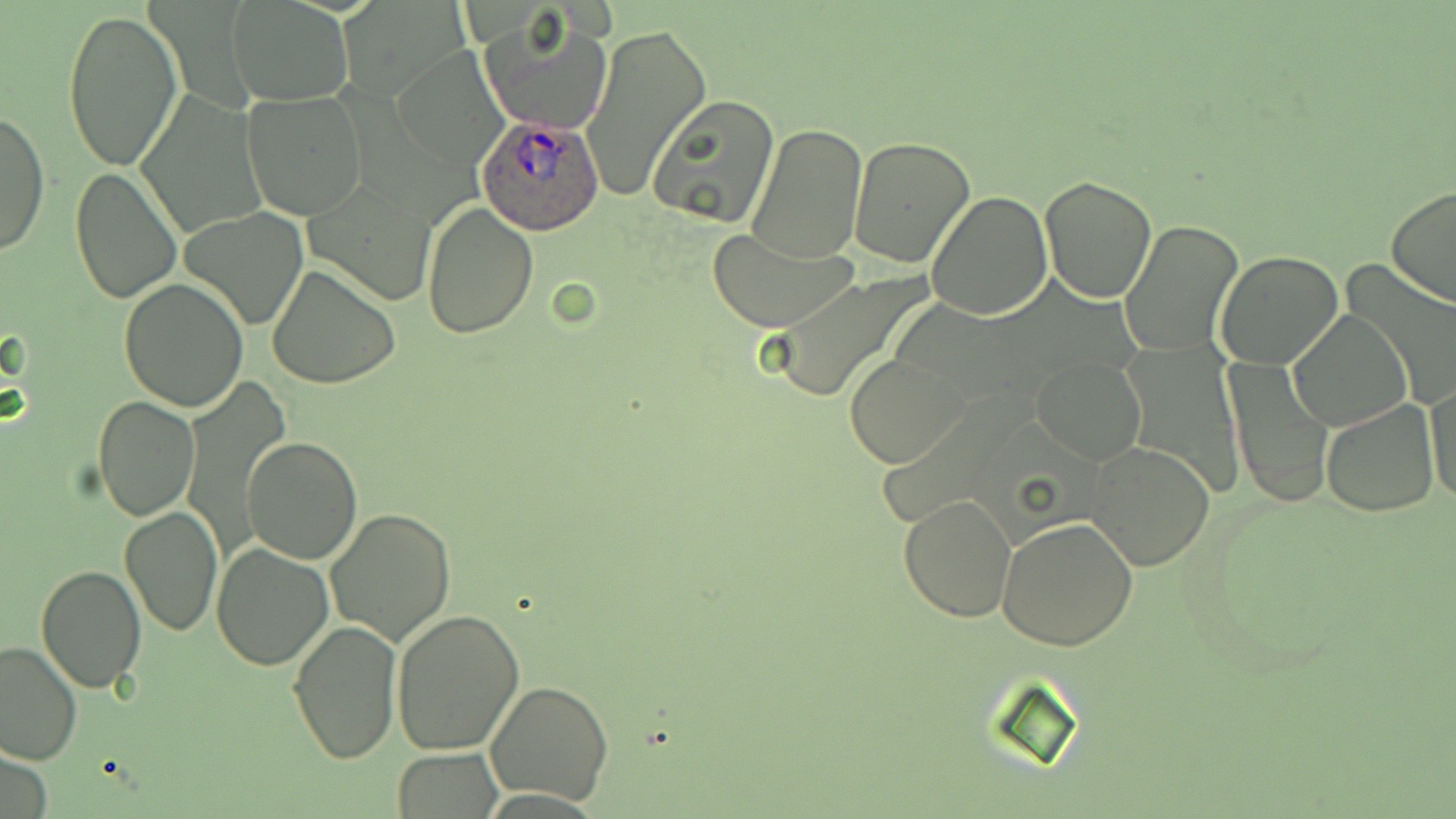

Summary:
  - Coordinate format: approximate bounding boxes as named x1/y1/x2/y2 corners in pixels
  - Plasmodium ovale-infected red blood cell locations: (x1=476, y1=113, x2=604, y2=236)
  - Uninfected red blood cell locations: (x1=229, y1=0, x2=352, y2=105), (x1=61, y1=5, x2=183, y2=173), (x1=481, y1=13, x2=613, y2=136), (x1=581, y1=20, x2=712, y2=204), (x1=242, y1=91, x2=368, y2=221), (x1=136, y1=92, x2=268, y2=242), (x1=647, y1=95, x2=783, y2=230), (x1=1, y1=110, x2=49, y2=255), (x1=747, y1=125, x2=868, y2=264), (x1=847, y1=135, x2=976, y2=268), (x1=68, y1=165, x2=183, y2=304), (x1=1039, y1=175, x2=1157, y2=303), (x1=305, y1=179, x2=438, y2=307), (x1=1385, y1=186, x2=1456, y2=309), (x1=926, y1=192, x2=1054, y2=320), (x1=421, y1=201, x2=539, y2=338), (x1=180, y1=208, x2=307, y2=331), (x1=1119, y1=219, x2=1244, y2=359), (x1=706, y1=230, x2=855, y2=332), (x1=1214, y1=250, x2=1345, y2=370), (x1=267, y1=263, x2=400, y2=389), (x1=765, y1=272, x2=932, y2=406), (x1=118, y1=277, x2=251, y2=412), (x1=1288, y1=309, x2=1412, y2=431), (x1=846, y1=354, x2=967, y2=469), (x1=1030, y1=354, x2=1147, y2=464), (x1=1223, y1=360, x2=1334, y2=506), (x1=1426, y1=380, x2=1455, y2=511), (x1=94, y1=394, x2=201, y2=521), (x1=1320, y1=400, x2=1439, y2=519), (x1=242, y1=435, x2=363, y2=564), (x1=1085, y1=439, x2=1216, y2=571), (x1=898, y1=493, x2=1018, y2=624), (x1=118, y1=504, x2=223, y2=636), (x1=325, y1=509, x2=457, y2=647), (x1=995, y1=516, x2=1138, y2=651), (x1=59, y1=524, x2=220, y2=668), (x1=210, y1=542, x2=335, y2=669), (x1=36, y1=564, x2=146, y2=693), (x1=391, y1=609, x2=525, y2=755), (x1=286, y1=619, x2=402, y2=764), (x1=0, y1=641, x2=83, y2=768), (x1=485, y1=680, x2=615, y2=806), (x1=393, y1=747, x2=501, y2=817)
  - Slide-level diagnosis: Plasmodium ovale
  - Field of view: single
  - Modality: light microscopy
  - Magnification: 1000x
  - Preparation: thin blood smear
  - Stain: May-Grünwald-Giemsa
  - Image size: 1456×819 pixels